Classify this cell by malaria status.
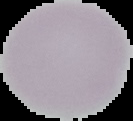
Uninfected.

Cell region segmented out of the field of view; the surrounding area is masked to black. Image is 133×121 pixels. From a thin blood smear.